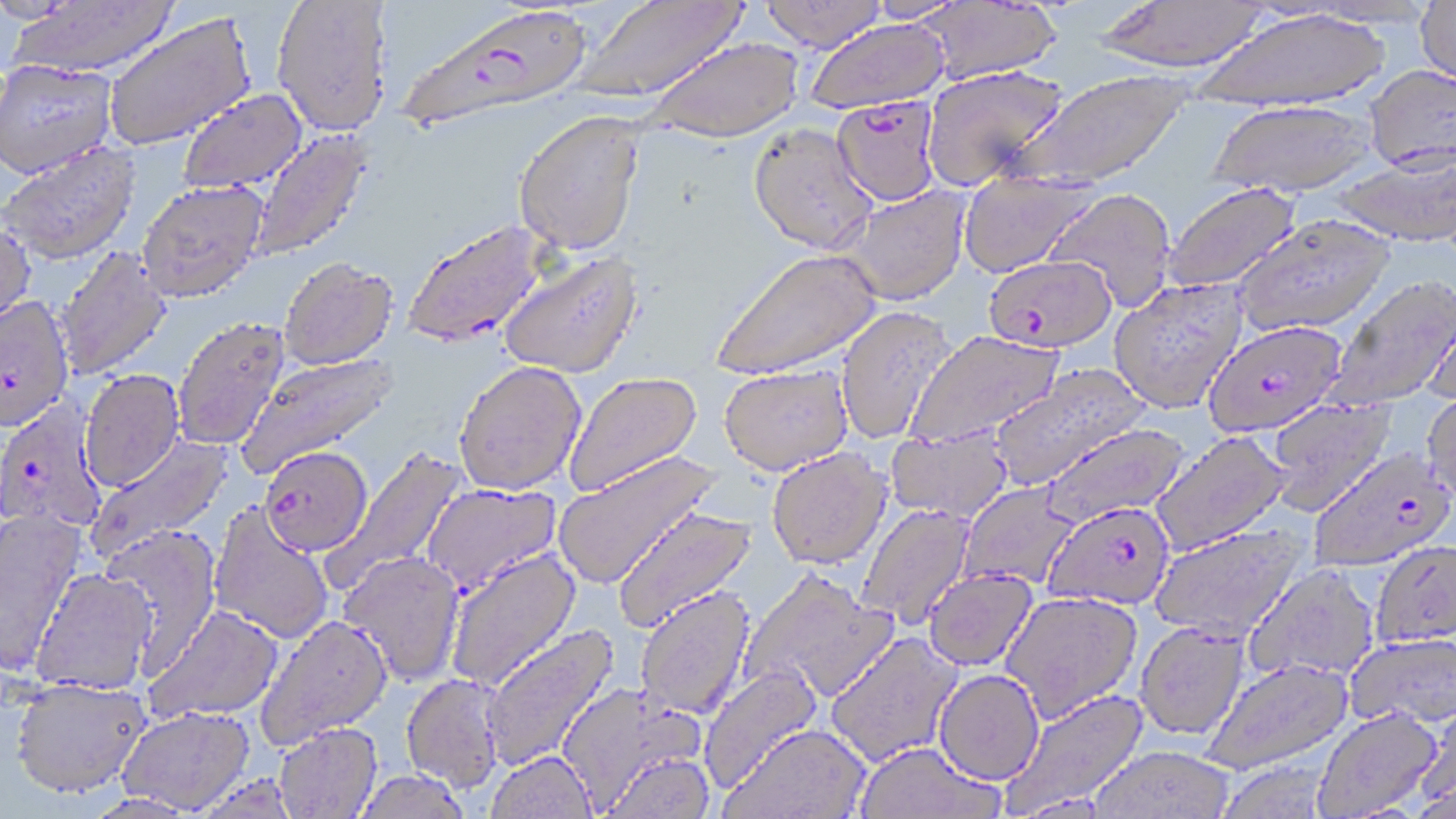
Summary:
  - Coordinate format: approximate bounding boxes as (x1, y1, x2, y2) in pixels
  - Uninfected red blood cell locations: (7, 0, 180, 82), (575, 0, 750, 104), (761, 0, 888, 52), (1093, 0, 1275, 75), (1415, 0, 1456, 93), (272, 1, 393, 140), (918, 1, 1060, 85), (1198, 8, 1391, 112), (105, 13, 257, 153), (805, 18, 950, 114), (644, 37, 801, 142), (0, 62, 118, 184), (1365, 63, 1456, 172), (922, 64, 1067, 191), (1016, 70, 1190, 191), (179, 90, 308, 195), (1210, 100, 1376, 197), (513, 113, 646, 257), (749, 122, 878, 255), (250, 128, 375, 263), (2, 144, 140, 268), (1335, 152, 1456, 247), (956, 170, 1096, 278), (1160, 181, 1302, 294), (136, 183, 268, 307), (842, 185, 971, 306), (1044, 187, 1176, 311), (1233, 215, 1394, 337), (0, 221, 36, 341), (54, 246, 173, 381), (711, 247, 883, 381), (497, 250, 644, 380), (279, 260, 398, 372), (1325, 274, 1456, 410), (1108, 279, 1248, 414), (1423, 294, 1456, 407), (835, 306, 956, 445), (174, 319, 290, 451), (906, 330, 1063, 447), (237, 350, 398, 478), (454, 363, 587, 496), (718, 364, 854, 475), (987, 364, 1149, 490), (79, 371, 186, 494), (563, 371, 703, 496), (1422, 388, 1456, 505), (1264, 397, 1397, 516), (1039, 422, 1191, 528), (885, 427, 1013, 523), (1149, 429, 1292, 556), (86, 433, 234, 561), (324, 446, 468, 589), (766, 447, 892, 568), (553, 451, 718, 589), (958, 482, 1081, 590), (423, 483, 562, 595), (856, 503, 976, 630), (208, 504, 333, 645), (613, 506, 757, 633), (0, 512, 86, 675), (1149, 522, 1309, 643), (100, 526, 223, 676), (1371, 539, 1456, 647), (445, 549, 581, 692), (338, 552, 465, 687), (1243, 563, 1380, 682), (922, 568, 1038, 671), (742, 569, 898, 704), (31, 571, 155, 696), (634, 585, 756, 722), (1000, 591, 1142, 721), (143, 604, 283, 724), (256, 616, 393, 750), (1135, 622, 1250, 740), (480, 623, 620, 772), (825, 631, 964, 768), (1345, 633, 1456, 730), (1204, 658, 1354, 775), (699, 662, 823, 793), (933, 669, 1044, 784), (401, 674, 506, 793), (9, 680, 152, 803), (555, 682, 704, 813), (1003, 689, 1149, 815), (1419, 695, 1456, 809), (1312, 705, 1444, 817), (117, 708, 256, 815), (723, 724, 869, 819), (274, 725, 382, 819), (854, 741, 1004, 819), (1090, 745, 1235, 819), (486, 750, 598, 818), (600, 750, 716, 818), (352, 771, 473, 819), (192, 776, 300, 819), (82, 795, 199, 818)
  - Plasmodium falciparum-infected red blood cell locations: (396, 6, 595, 134), (831, 95, 943, 207), (404, 220, 551, 349), (983, 255, 1116, 353), (0, 298, 74, 435), (1202, 320, 1347, 437), (0, 399, 106, 533), (1309, 446, 1454, 570), (258, 449, 372, 558), (1043, 501, 1176, 610)
  - Slide-level diagnosis: Plasmodium falciparum
  - Stain: May-Grünwald-Giemsa
  - Modality: light microscopy
  - Preparation: thin blood film
  - Image size: 1456×819 pixels
  - Field of view: one of a larger specimen
  - Magnification: 1000x